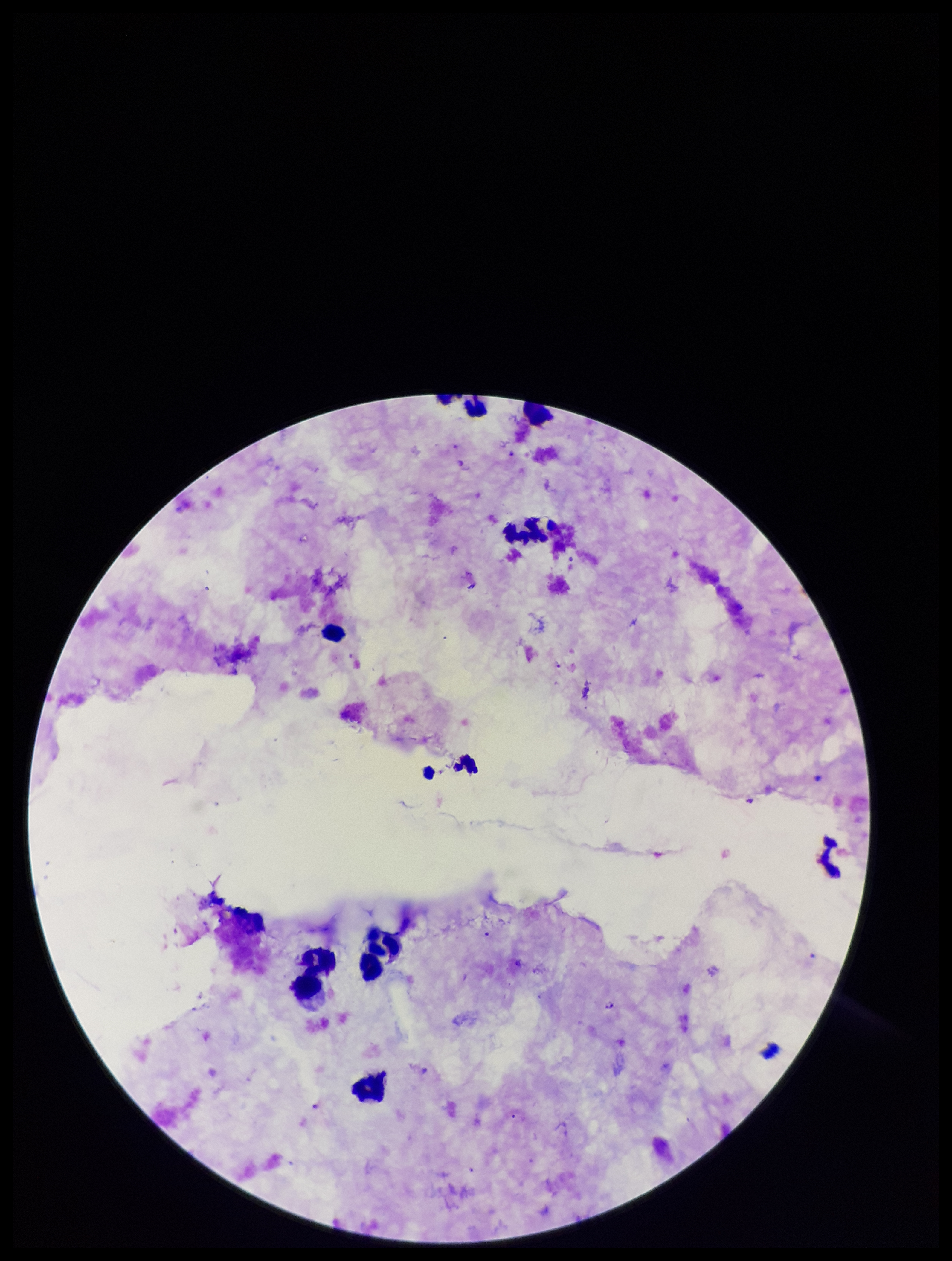
Species reported for this patient: Plasmodium falciparum. Patient malaria status: infected. Smartphone photograph taken through the eyepiece of a microscope. Preparation: thick smear. Image is 952×1261 pixels. Plasmodium parasites: seen. Parasite count: 2. One field from this slide. Stained with Giemsa. Leukocyte count: 9.